Name the cell type shown.
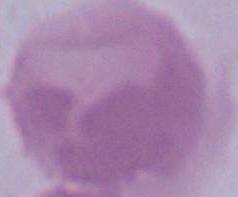
This is an erythrocyte.

Summary:
  - Modality: photomicrograph
  - Magnification: 1000x